Identify the blood parasite species.
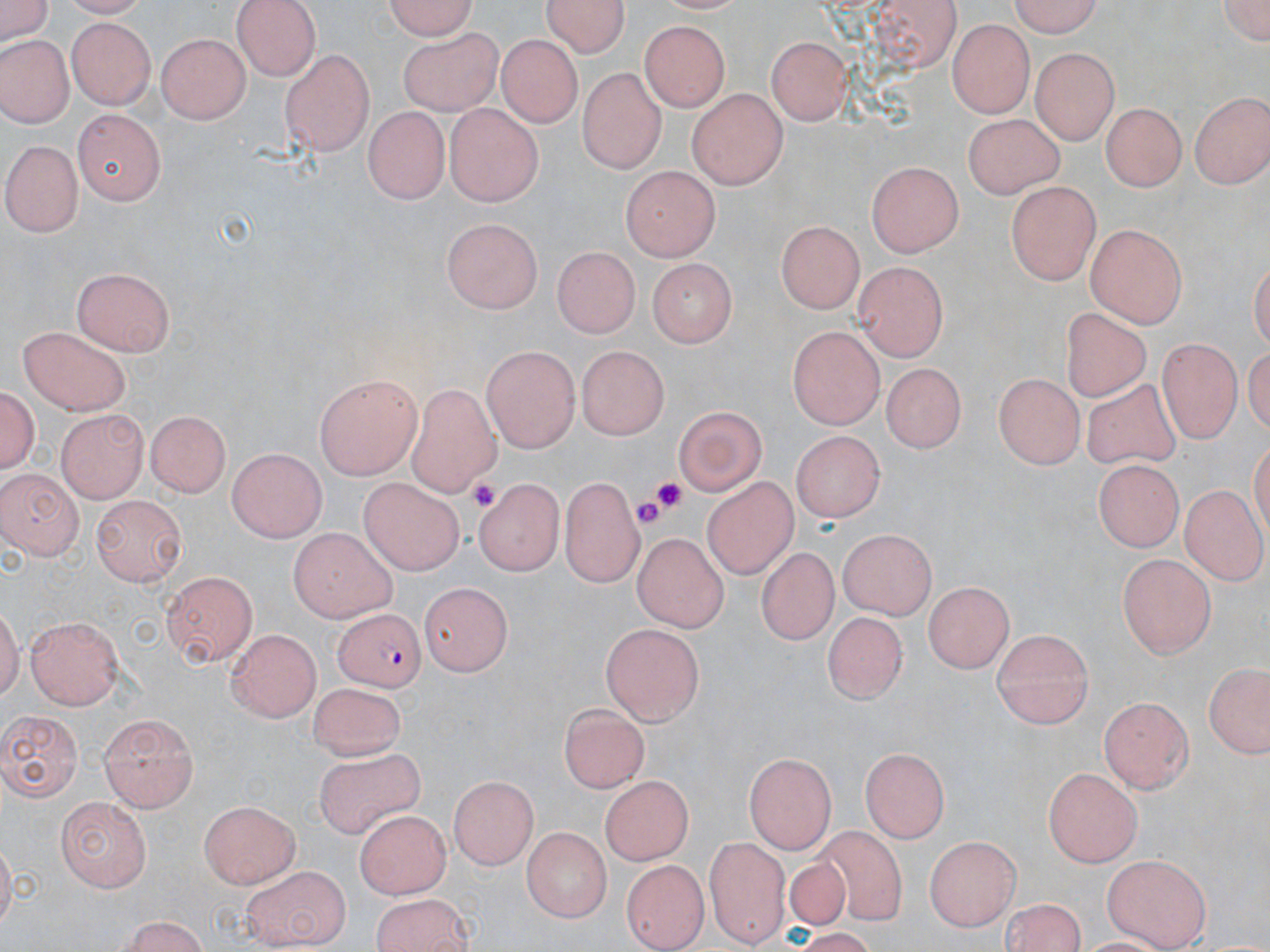
Plasmodium falciparum.

Approximate bounding boxes as (x1, y1, x2, y2) in pixels. Uninfected red blood cell locations: (0, 0, 58, 42), (382, 0, 482, 39), (869, 0, 963, 70), (1003, 0, 1104, 35), (1219, 0, 1269, 47), (234, 1, 322, 78), (543, 1, 633, 55), (69, 18, 155, 107), (948, 19, 1031, 116), (641, 21, 729, 109), (397, 30, 502, 114), (157, 32, 251, 124), (768, 36, 856, 127), (0, 37, 68, 127), (498, 37, 581, 127), (278, 48, 371, 153), (1032, 49, 1121, 140), (576, 66, 664, 172), (688, 89, 785, 188), (1188, 90, 1269, 188), (364, 103, 452, 201), (439, 103, 544, 207), (1099, 103, 1188, 192), (74, 108, 168, 206), (962, 111, 1068, 198), (5, 139, 83, 234), (865, 159, 964, 255), (619, 167, 719, 262), (1007, 183, 1098, 288), (444, 219, 540, 312), (776, 219, 863, 313), (1084, 222, 1189, 324), (554, 245, 639, 339), (644, 257, 739, 347), (853, 260, 946, 359), (74, 266, 178, 353), (1060, 308, 1154, 404), (20, 325, 133, 416), (788, 326, 882, 429), (1157, 338, 1241, 445), (576, 344, 665, 440), (480, 346, 582, 449), (879, 359, 968, 446), (992, 372, 1082, 471), (313, 376, 423, 480), (1082, 378, 1184, 470), (404, 384, 501, 493), (2, 385, 39, 483), (674, 403, 769, 493), (57, 410, 146, 503), (146, 410, 233, 495), (787, 432, 887, 523), (225, 449, 329, 538), (1095, 458, 1185, 550), (0, 466, 83, 555), (559, 475, 646, 584), (701, 475, 801, 584), (359, 478, 467, 572), (472, 479, 561, 573), (1180, 486, 1267, 581), (93, 494, 187, 584), (286, 528, 397, 620), (839, 529, 939, 619), (634, 531, 728, 632), (755, 546, 841, 645), (1117, 550, 1216, 658), (163, 570, 259, 667), (421, 579, 515, 673), (923, 581, 1017, 674), (821, 611, 905, 710), (28, 617, 125, 707), (598, 622, 702, 727), (225, 627, 319, 722), (992, 628, 1094, 729), (1204, 659, 1270, 759), (306, 682, 405, 760), (1097, 697, 1198, 791), (555, 704, 647, 795), (99, 708, 196, 809), (0, 711, 81, 804), (862, 747, 949, 839), (313, 749, 427, 843), (745, 754, 837, 851), (1043, 767, 1142, 866), (449, 775, 540, 869), (600, 775, 691, 867), (199, 796, 299, 888), (54, 798, 150, 889), (357, 807, 452, 896), (811, 821, 912, 925), (520, 826, 610, 921), (925, 833, 1017, 931), (705, 834, 790, 942), (782, 856, 855, 928), (1103, 857, 1209, 949), (622, 859, 709, 949), (238, 863, 348, 948), (368, 891, 475, 952), (999, 898, 1090, 952), (111, 918, 214, 951). Plasmodium falciparum-infected red blood cell locations: (334, 604, 428, 688). Platelet locations: (652, 477, 690, 511), (471, 478, 500, 510), (632, 500, 669, 530). Optical microscopy. Image is 1270×952 pixels. Captured at 1000x magnification. Thin blood film. May-Grünwald-Giemsa stain. One field of a larger specimen.